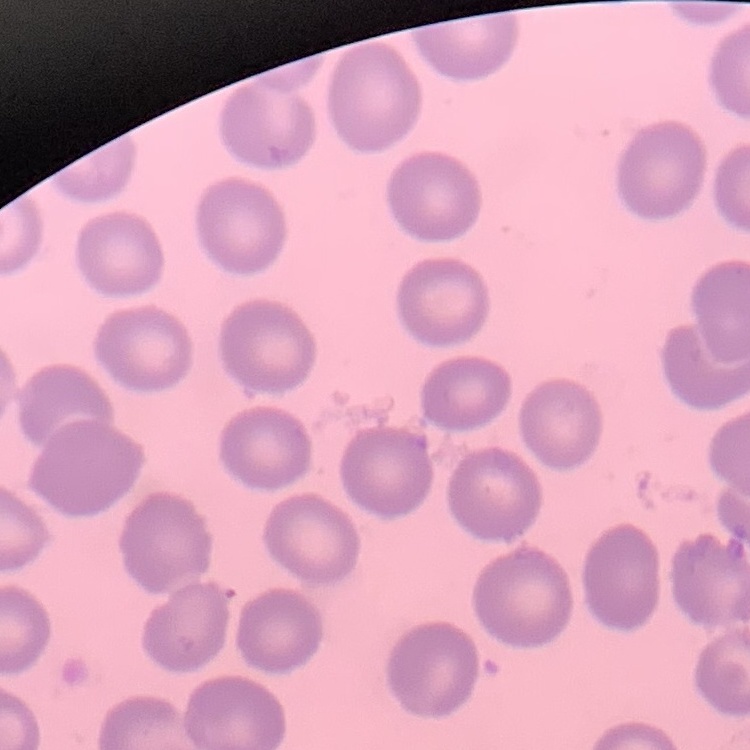
{
  "erythrocyte_morphology": "no rouleaux formation",
  "stain": "Field's or Giemsa",
  "preparation": "thin blood smear",
  "image_type": "one tile cut from a larger photomicrograph"
}